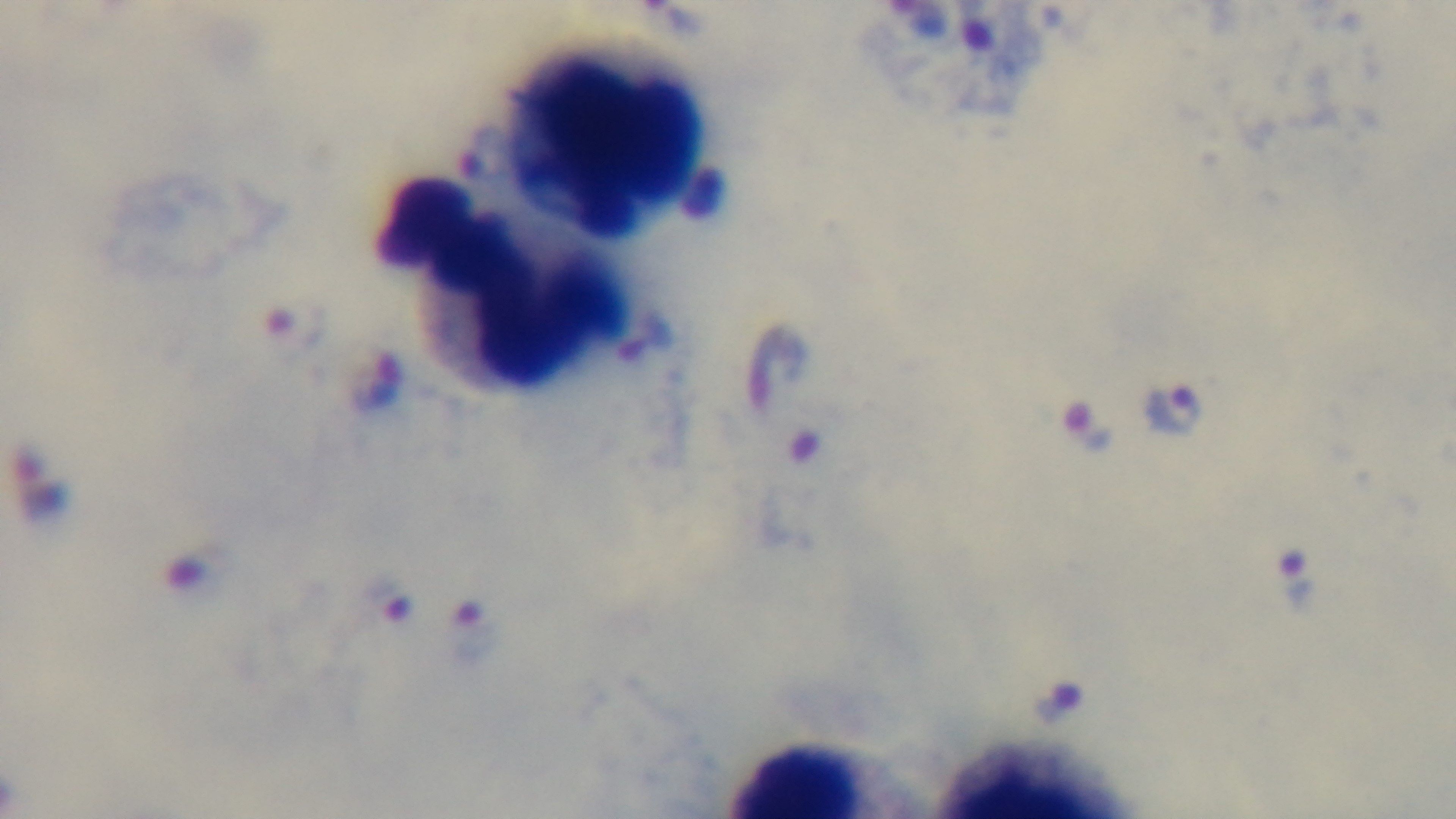
malaria status = positive
stain = Giemsa
preparation = thick
modality = light microscopy
capture = mounted 4K digital camera
field of view = single
objective = 100x oil immersion